Give the extent of all uninfected red blood cells.
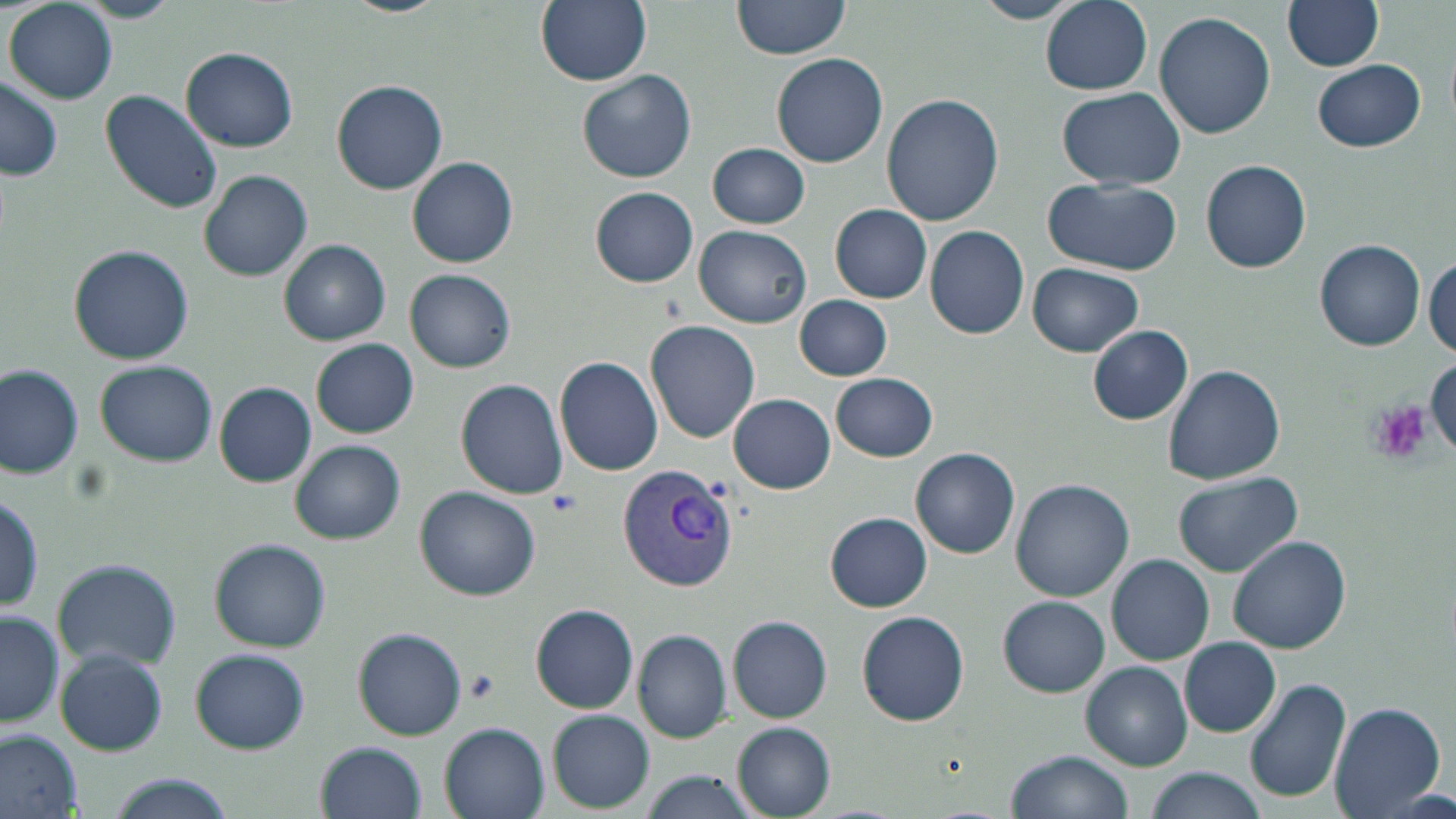

Approximate bounding boxes as named x1/y1/x2/y2 corners in pixels.
Uninfected red blood cells: (x1=77, y1=0, x2=182, y2=23), (x1=339, y1=0, x2=448, y2=17), (x1=535, y1=0, x2=651, y2=86), (x1=972, y1=0, x2=1085, y2=24), (x1=1041, y1=0, x2=1152, y2=94), (x1=1284, y1=0, x2=1385, y2=72), (x1=7, y1=1, x2=117, y2=104), (x1=730, y1=1, x2=852, y2=63), (x1=1153, y1=11, x2=1275, y2=139), (x1=181, y1=47, x2=298, y2=152), (x1=771, y1=52, x2=888, y2=168), (x1=1313, y1=59, x2=1427, y2=152), (x1=577, y1=69, x2=697, y2=183), (x1=0, y1=77, x2=63, y2=181), (x1=332, y1=80, x2=447, y2=193), (x1=100, y1=89, x2=223, y2=214), (x1=1056, y1=89, x2=1187, y2=192), (x1=880, y1=92, x2=1003, y2=226), (x1=707, y1=143, x2=809, y2=229), (x1=409, y1=156, x2=518, y2=269), (x1=1199, y1=160, x2=1313, y2=273), (x1=198, y1=169, x2=315, y2=281), (x1=1043, y1=178, x2=1181, y2=275), (x1=591, y1=187, x2=697, y2=286), (x1=830, y1=204, x2=933, y2=303), (x1=925, y1=225, x2=1029, y2=339), (x1=696, y1=226, x2=811, y2=327), (x1=280, y1=240, x2=390, y2=345), (x1=1315, y1=240, x2=1427, y2=349), (x1=70, y1=246, x2=194, y2=365), (x1=1427, y1=257, x2=1455, y2=359), (x1=1028, y1=263, x2=1144, y2=356), (x1=406, y1=270, x2=514, y2=372), (x1=794, y1=294, x2=892, y2=381), (x1=645, y1=321, x2=759, y2=441), (x1=1087, y1=325, x2=1193, y2=424), (x1=312, y1=338, x2=419, y2=437), (x1=555, y1=356, x2=664, y2=476), (x1=1427, y1=356, x2=1456, y2=453), (x1=95, y1=360, x2=217, y2=467), (x1=1, y1=363, x2=83, y2=480), (x1=1163, y1=364, x2=1286, y2=484), (x1=830, y1=372, x2=938, y2=462), (x1=455, y1=379, x2=569, y2=499), (x1=214, y1=382, x2=316, y2=486), (x1=731, y1=383, x2=940, y2=479), (x1=729, y1=394, x2=836, y2=494), (x1=291, y1=440, x2=405, y2=543), (x1=911, y1=447, x2=1020, y2=558), (x1=1172, y1=473, x2=1302, y2=578), (x1=1010, y1=479, x2=1133, y2=602), (x1=416, y1=486, x2=541, y2=601), (x1=0, y1=487, x2=43, y2=615), (x1=825, y1=512, x2=932, y2=612), (x1=1228, y1=536, x2=1350, y2=654), (x1=211, y1=540, x2=329, y2=652), (x1=1108, y1=553, x2=1215, y2=665), (x1=53, y1=559, x2=180, y2=672), (x1=1000, y1=597, x2=1109, y2=695), (x1=530, y1=605, x2=639, y2=713), (x1=0, y1=608, x2=62, y2=730), (x1=856, y1=610, x2=969, y2=726), (x1=729, y1=615, x2=833, y2=723), (x1=354, y1=627, x2=466, y2=740), (x1=634, y1=629, x2=731, y2=742), (x1=1180, y1=637, x2=1279, y2=737), (x1=190, y1=648, x2=311, y2=753), (x1=55, y1=649, x2=168, y2=756), (x1=1081, y1=661, x2=1190, y2=771), (x1=1244, y1=678, x2=1352, y2=805), (x1=1327, y1=701, x2=1445, y2=818), (x1=548, y1=710, x2=654, y2=811), (x1=440, y1=722, x2=551, y2=819), (x1=733, y1=723, x2=836, y2=816), (x1=0, y1=730, x2=81, y2=816), (x1=314, y1=741, x2=426, y2=819), (x1=1008, y1=749, x2=1133, y2=819), (x1=1147, y1=767, x2=1269, y2=819), (x1=640, y1=772, x2=760, y2=819), (x1=104, y1=777, x2=236, y2=819).

Plasmodium vivax-infected red blood cell locations: (x1=617, y1=465, x2=738, y2=593). Platelet locations: (x1=1369, y1=399, x2=1432, y2=465), (x1=546, y1=490, x2=580, y2=516), (x1=464, y1=670, x2=498, y2=703). Slide-level diagnosis: Plasmodium vivax. Thin blood smear. Light microscopy. Single field of view. May-Grünwald-Giemsa-stained preparation. 1000x magnification. Image is 1456×819 pixels.